Locate every Babesia divergens-infected red blood cell.
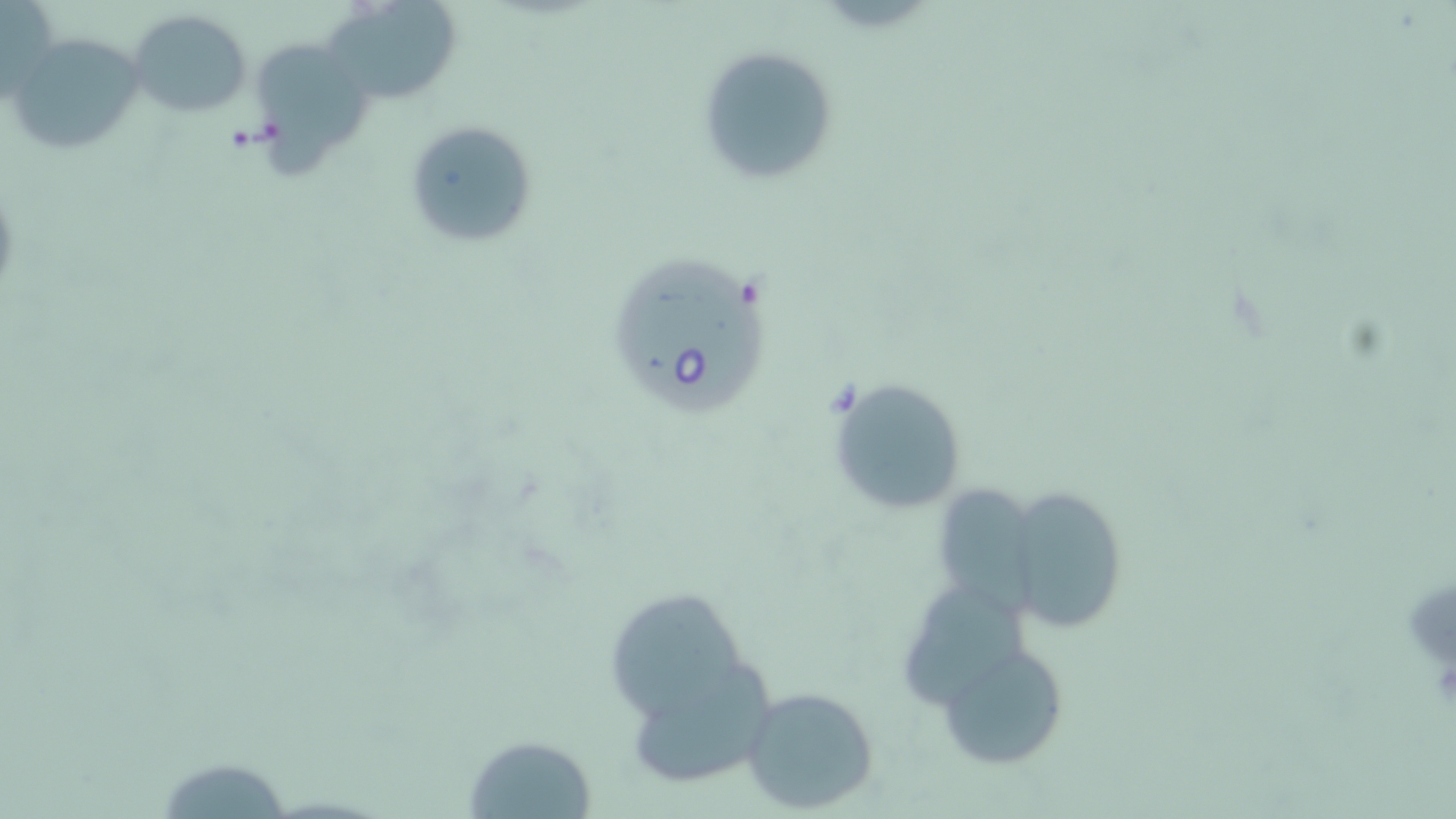

Approximate bounding boxes as named x1/y1/x2/y2 corners in pixels.
Babesia divergens-infected red blood cells: (x1=615, y1=252, x2=770, y2=416).

slide-level diagnosis = Babesia divergens
stain = May-Grünwald-Giemsa
field of view = single
magnification = 1000x
uninfected red blood cell locations = approximate bounding boxes as named x1/y1/x2/y2 corners in pixels: (x1=1, y1=0, x2=60, y2=103), (x1=323, y1=1, x2=461, y2=105), (x1=129, y1=11, x2=252, y2=116), (x1=11, y1=34, x2=143, y2=156), (x1=254, y1=41, x2=377, y2=177), (x1=697, y1=46, x2=839, y2=187), (x1=403, y1=119, x2=539, y2=251), (x1=828, y1=376, x2=969, y2=517), (x1=940, y1=482, x2=1033, y2=622), (x1=1004, y1=487, x2=1127, y2=634), (x1=906, y1=582, x2=1037, y2=703), (x1=612, y1=590, x2=748, y2=729), (x1=939, y1=640, x2=1070, y2=771), (x1=739, y1=684, x2=881, y2=814), (x1=464, y1=734, x2=598, y2=816)
modality = light microscopy
image size = 1456×819 pixels
preparation = thin blood smear